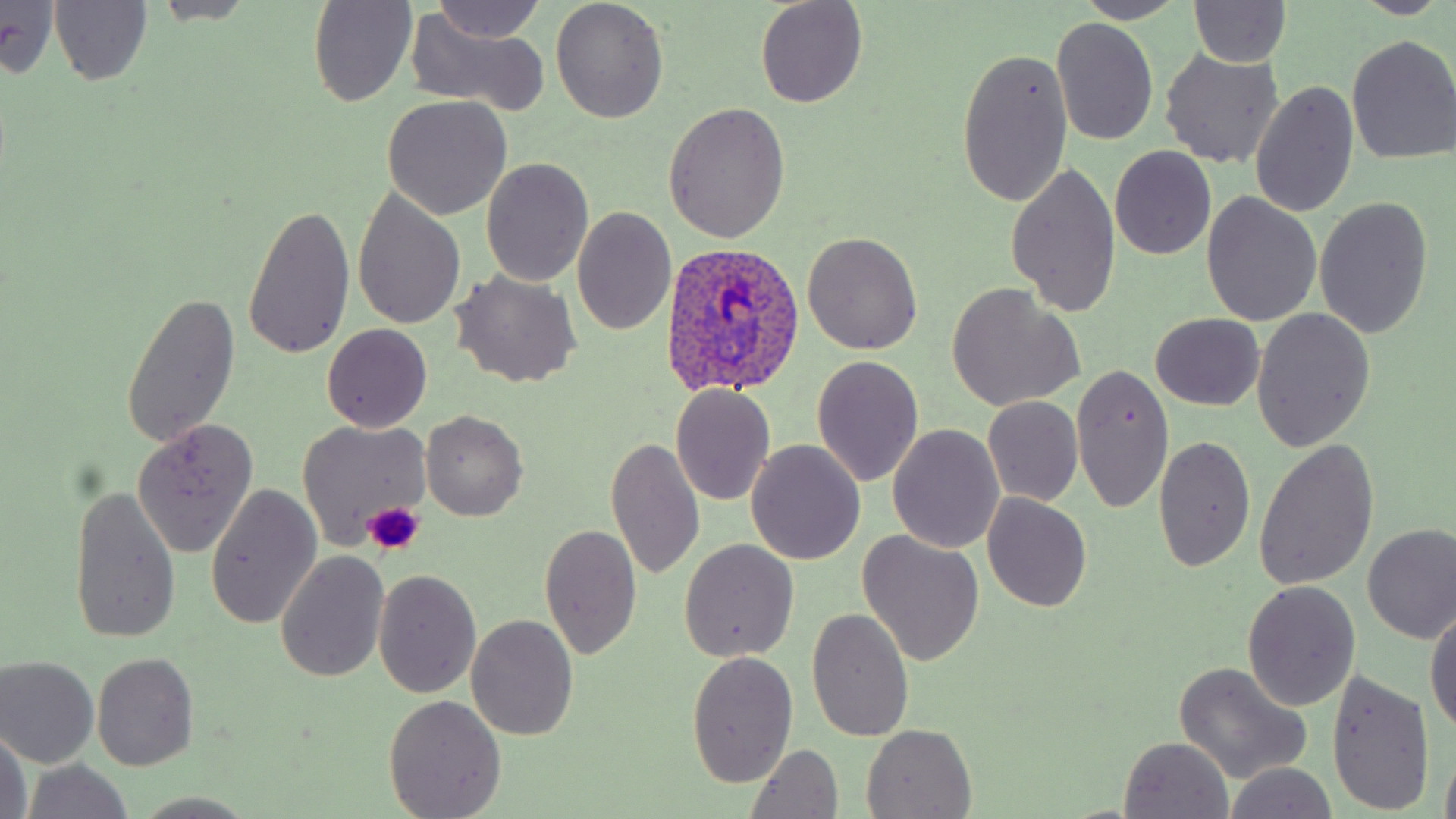
slide-level diagnosis = Plasmodium ovale
image size = 1456×819 pixels
preparation = thin blood smear
Plasmodium ovale-infected red blood cell locations = approximate bounding boxes as (x1, y1, x2, y2) in pixels: (664, 243, 809, 397)
platelet locations = approximate bounding boxes as (x1, y1, x2, y2) in pixels: (362, 502, 424, 555)
field of view = one of a larger specimen
modality = optical microscopy
uninfected red blood cell locations = approximate bounding boxes as (x1, y1, x2, y2) in pixels: (308, 0, 417, 108), (428, 0, 546, 45), (550, 0, 670, 122), (754, 0, 869, 109), (1076, 0, 1187, 25), (1341, 0, 1450, 19), (149, 1, 260, 26), (48, 2, 152, 87), (1189, 2, 1292, 70), (0, 3, 61, 77), (403, 9, 553, 113), (1050, 17, 1159, 147), (1346, 35, 1456, 164), (955, 46, 1071, 209), (1159, 49, 1284, 167), (1249, 81, 1359, 218), (381, 97, 513, 220), (663, 101, 791, 243), (1109, 145, 1216, 259), (480, 158, 594, 287), (1006, 160, 1122, 319), (352, 187, 465, 330), (1201, 191, 1321, 327), (1314, 197, 1433, 338), (242, 202, 354, 359), (572, 207, 676, 338), (802, 231, 923, 354), (450, 270, 583, 388), (947, 284, 1084, 411), (122, 292, 240, 449), (1251, 310, 1375, 452), (1151, 313, 1263, 410), (322, 323, 433, 431), (811, 355, 924, 486), (1070, 362, 1174, 515), (670, 385, 775, 505), (983, 397, 1083, 505), (420, 410, 528, 521), (298, 419, 430, 549), (131, 420, 261, 557), (888, 424, 1004, 554), (607, 434, 705, 581), (1154, 435, 1256, 573), (1254, 438, 1379, 590), (747, 442, 866, 567), (204, 484, 322, 630), (69, 485, 182, 647), (981, 492, 1092, 613), (539, 521, 641, 661), (1362, 523, 1456, 644), (857, 531, 985, 668), (678, 539, 799, 662), (277, 550, 389, 682), (373, 569, 481, 697), (1242, 580, 1361, 709), (1426, 603, 1456, 738), (806, 607, 915, 743), (466, 615, 578, 739), (685, 650, 800, 788), (91, 654, 199, 770), (1, 656, 100, 768), (1174, 661, 1312, 784), (1326, 672, 1435, 816), (383, 695, 506, 818), (861, 723, 978, 817), (0, 725, 31, 819), (1118, 737, 1235, 818), (745, 745, 845, 818), (20, 761, 135, 819), (1221, 763, 1338, 819), (134, 792, 258, 818)
stain = May-Grünwald-Giemsa
magnification = 1000x